Report the malaria status of this cell.
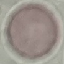

It is uninfected.

Thin blood smear. Giemsa stain. Acquired by smartphone through the microscope eyepiece. Cell patch, automatically extracted from a larger field of view and resized to 64 × 64 pixels.